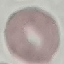
Summary:
  - Malaria status: uninfected
  - Stain: Giemsa
  - Preparation: thin blood film
  - Image type: automatically extracted cell patch, resized to 64 × 64 pixels
  - Capture: smartphone through the microscope eyepiece